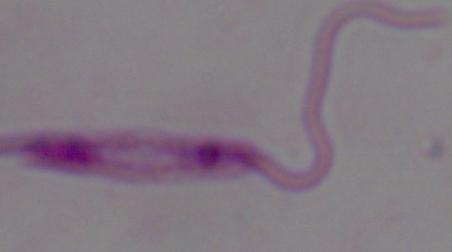

{
  "magnification": "1000x",
  "modality": "micrograph",
  "identification": "Leishmania"
}